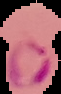
Result: malaria parasites identified. Image is 61×94 pixels. The area outside the segmented cell region is set to black. From a thin blood film.